Assess this cell for malaria.
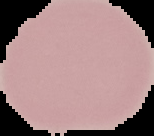
It is uninfected.

Image is 154×136 pixels. From a thin blood smear. Segmented cell region on a black background.